Comment on the morphology of the erythrocytes.
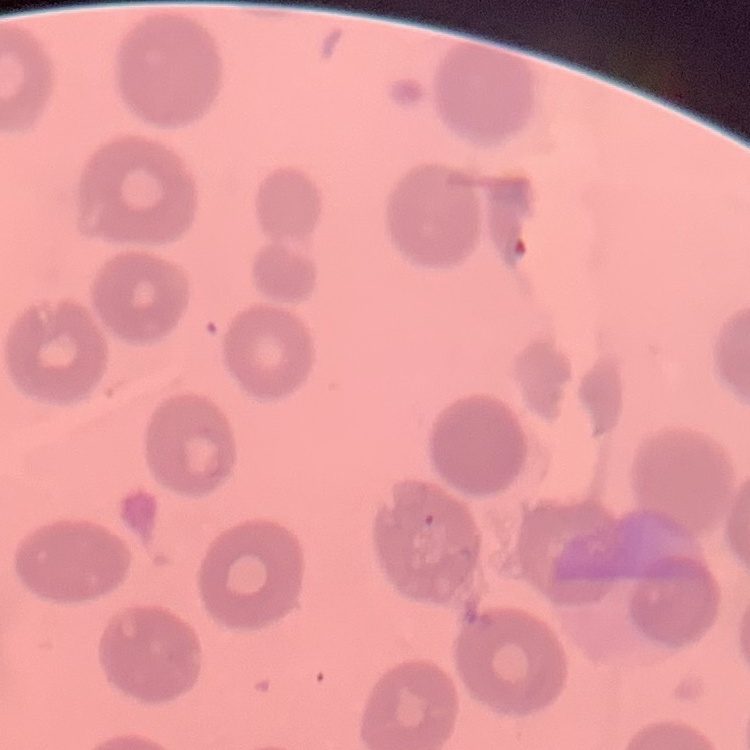

They show no rouleaux formation.

Summary:
  - Stain: Field's or Giemsa
  - Image type: one tile cut from a larger photomicrograph
  - Preparation: thin blood smear